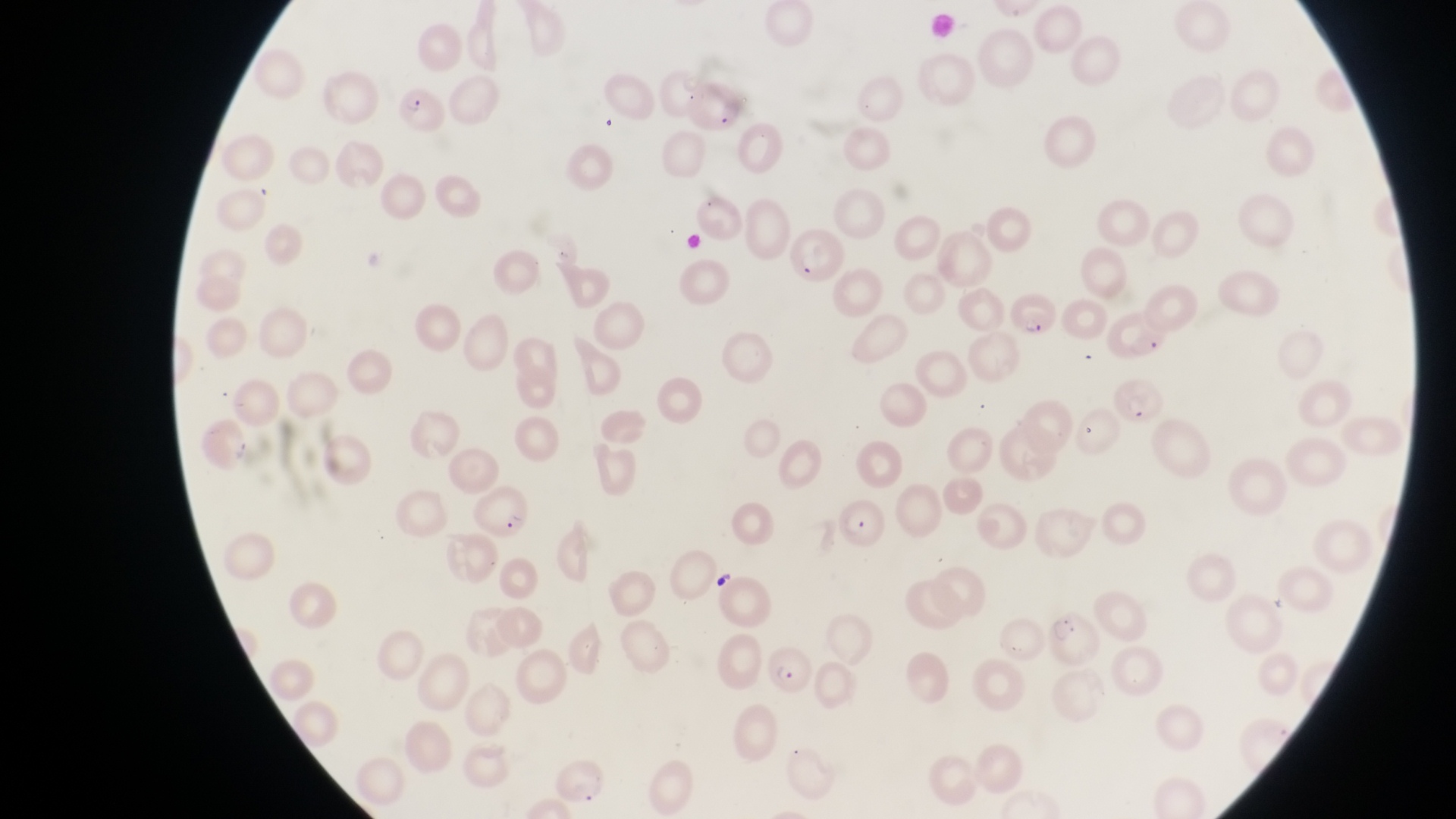

Approximate bounding boxes as {left, top, right, bottom} in pixels.
Summary:
  - Parasitised red blood cell locations: {789, 228, 844, 289}, {1012, 285, 1062, 340}, {1109, 370, 1165, 429}, {473, 482, 534, 542}, {830, 495, 883, 550}, {1050, 605, 1102, 666}, {764, 642, 814, 697}, {549, 756, 607, 814}
  - Preparation: thin blood film
  - Country: Uganda
  - Image size: 1456×819 pixels
  - Magnification: 1000x
  - Capture: smartphone photograph through the eyepiece of an Olympus CX-23 microscope
  - Field of view: single